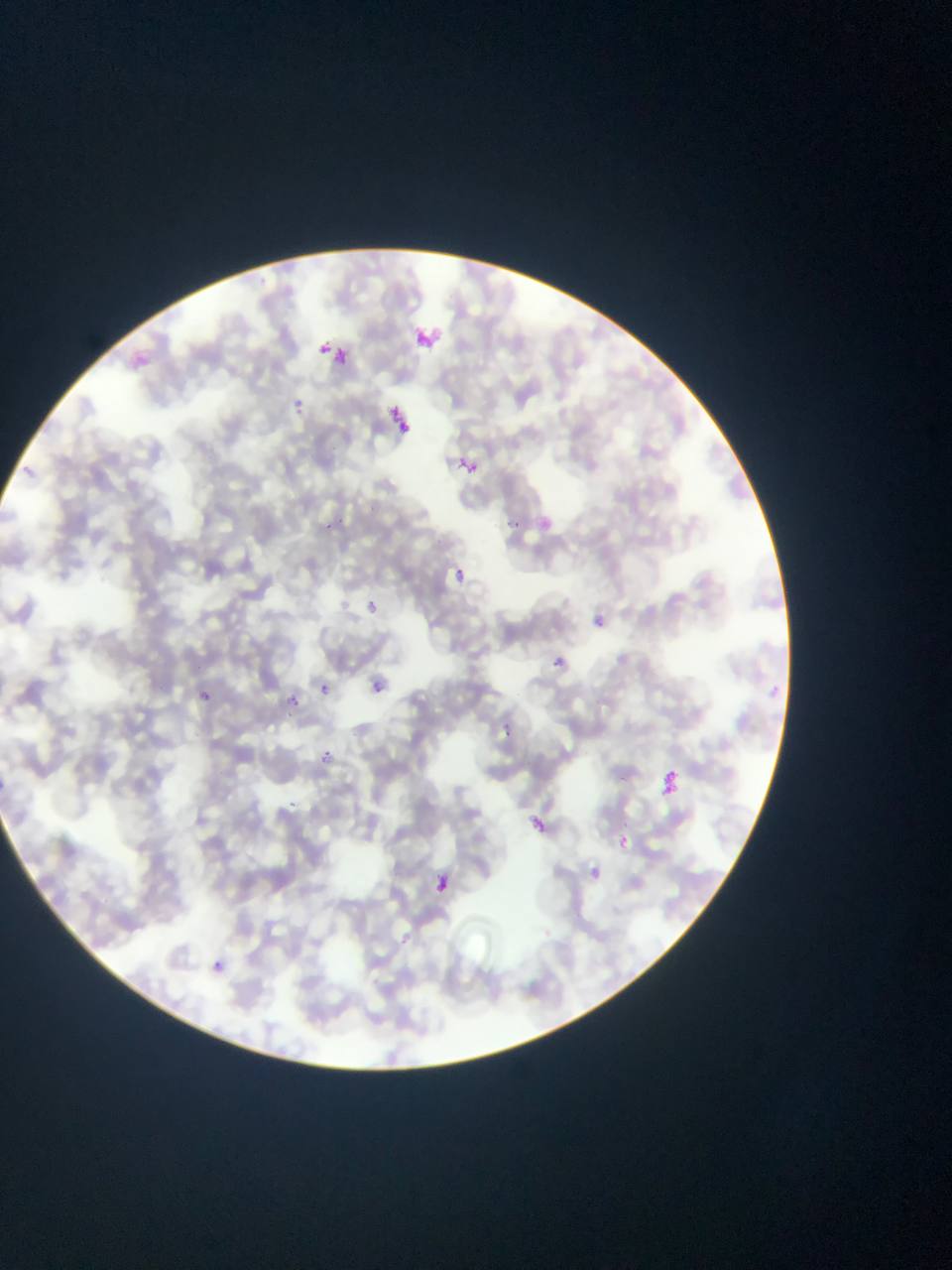
Approximate bounding boxes as (left, top, right, bottom) in pixels.
Summary:
  - Plasmodium parasite locations: (415, 324, 444, 356), (314, 340, 336, 352), (331, 346, 345, 363), (386, 401, 418, 438), (454, 456, 483, 478), (503, 515, 535, 539), (316, 522, 330, 532), (450, 564, 472, 580), (358, 590, 387, 617), (594, 615, 607, 629), (553, 655, 567, 667), (364, 677, 398, 702), (316, 682, 337, 708), (198, 685, 214, 708), (289, 694, 301, 706), (497, 724, 520, 740), (322, 745, 339, 767), (656, 771, 681, 797), (532, 817, 546, 831), (617, 831, 634, 853), (590, 867, 602, 879), (437, 871, 446, 895), (210, 956, 227, 970)
  - Field of view: single
  - Country: Ghana
  - Capture: mobile-phone photograph through a microscope
  - Image size: 952×1270 pixels
  - Preparation: thin blood film